Locate every leukocyte (white blood cell).
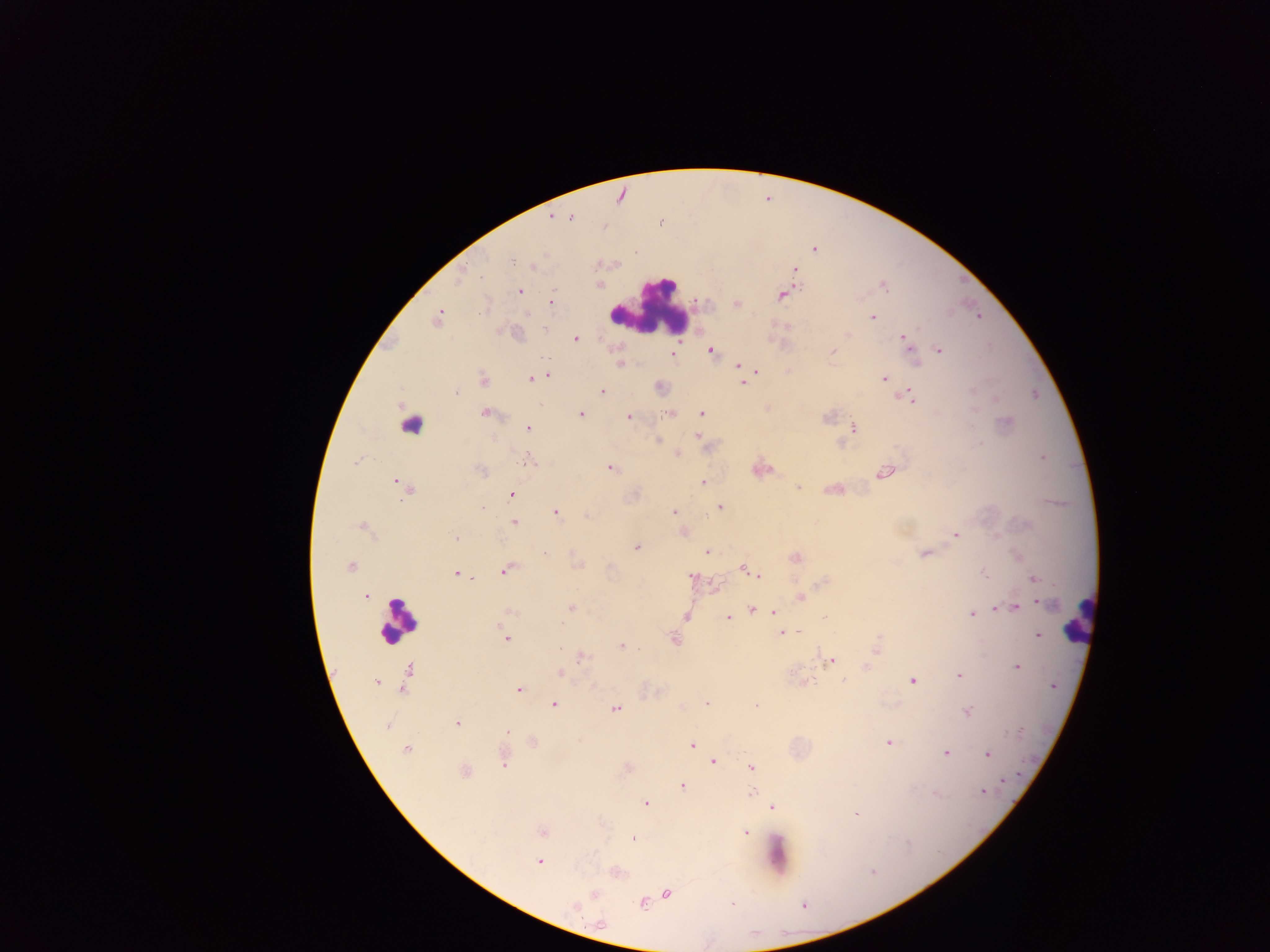

Approximate centers as x y in pixels.
Leukocytes: 647 307; 411 421; 1079 619; 398 620.

Summary:
  - Plasmodium parasite locations: 570 218; 814 249; 634 252; 513 262; 795 269; 460 277; 885 287; 519 291; 782 294; 551 301; 737 303; 485 307; 437 317; 873 317; 545 329; 848 335; 576 338; 905 340; 910 345; 939 350; 710 351; 833 351; 673 354; 544 358; 620 364; 739 365; 756 371; 548 376; 884 378; 483 379; 531 379; 743 383; 973 390; 601 391; 456 393; 909 396; 486 413; 701 413; 581 414; 668 414; 828 416; 628 417; 1006 422; 854 427; 527 428; 698 436; 658 441; 979 443; 678 453; 1042 458; 355 462; 526 462; 611 468; 481 471; 886 473; 396 481; 703 482; 798 488; 406 489; 511 494; 482 507; 720 507; 556 512; 673 512; 587 516; 514 522; 362 526; 955 534; 455 539; 636 547; 545 553; 707 553; 924 554; 796 557; 350 566; 744 568; 506 571; 750 571; 984 572; 456 574; 759 576; 692 577; 1034 579; 365 596; 801 596; 1043 603; 571 608; 1015 608; 752 609; 997 609; 510 611; 773 612; 972 613; 686 616; 728 617; 824 617; 789 632; 798 632; 781 633; 1038 635; 505 638; 674 640; 878 644; 622 646; 559 649; 876 650; 582 657; 831 660; 1017 667; 408 669; 560 672; 958 675; 844 681; 912 681; 375 682; 402 688; 518 690; 706 703; 554 704; 756 705; 616 708; 967 712; 458 723; 387 726; 507 731; 888 743; 692 746; 407 749; 945 753; 988 755; 714 762; 504 763; 751 767; 465 771; 1004 781; 683 786; 983 791; 751 792; 936 794; 645 803; 772 808; 855 814; 542 832; 746 833; 633 839; 907 842; 539 862; 872 872; 666 894; 593 895; 643 903; 731 903; 573 908; 599 922
  - Field of view: single
  - Country: Ghana
  - Image size: 1270×952 pixels
  - Capture: mobile-phone photograph through a microscope
  - Preparation: thick blood smear